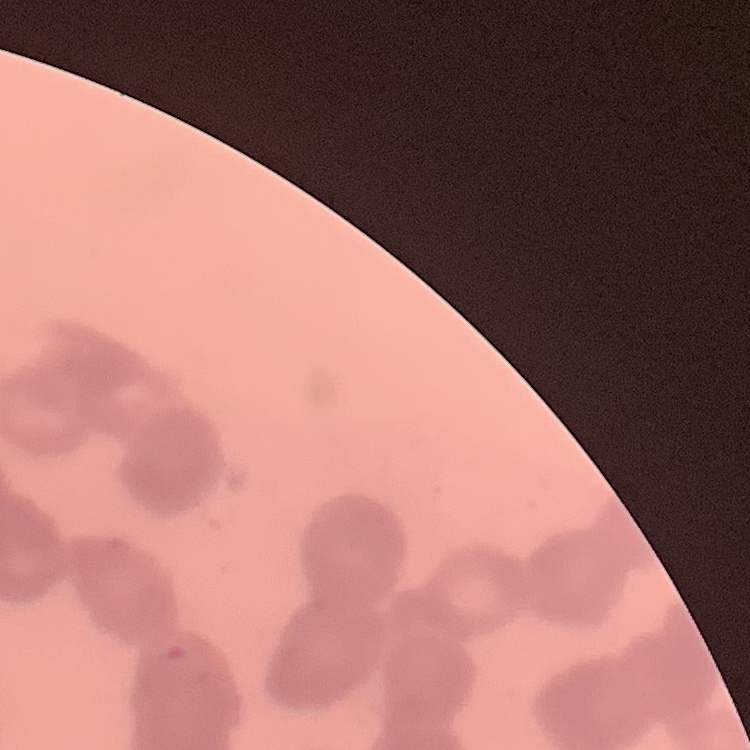
erythrocyte morphology = rouleaux formation
stain = Field's or Giemsa
image type = one tile cut from a larger photomicrograph
preparation = thin blood film